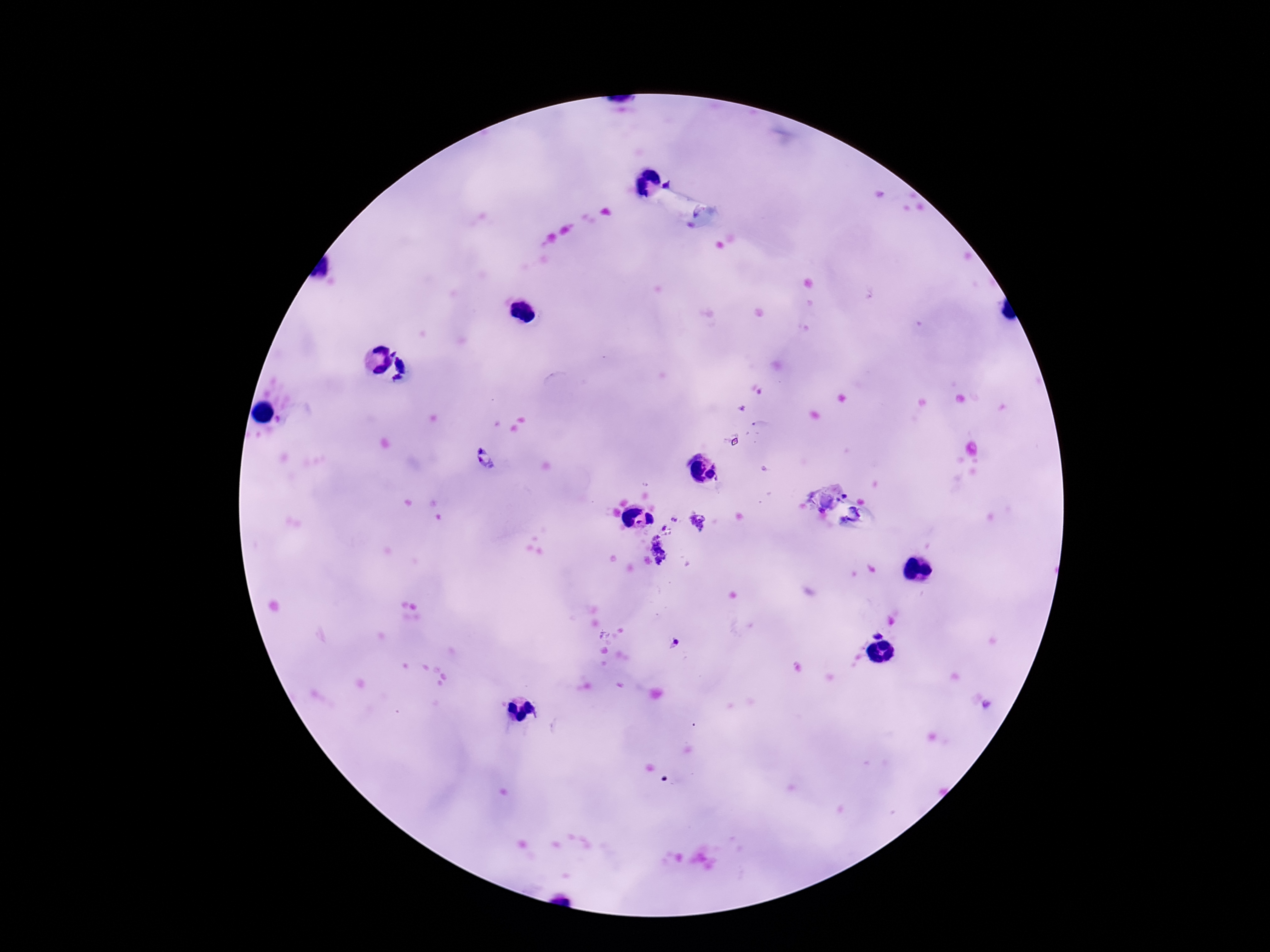

Approximate object centers, in pixels from the top-left corner.
Summary:
  - Plasmodium parasite locations: (x=406, y=371), (x=485, y=459), (x=674, y=519), (x=698, y=522), (x=664, y=527), (x=660, y=550), (x=877, y=634), (x=674, y=643)
  - Magnification: 100x
  - Preparation: thick blood film
  - Capture: smartphone camera through the microscope eyepiece
  - Stain: Giemsa
  - Field of view: single
  - Patient malaria status: infected
  - Image size: 1270×952 pixels